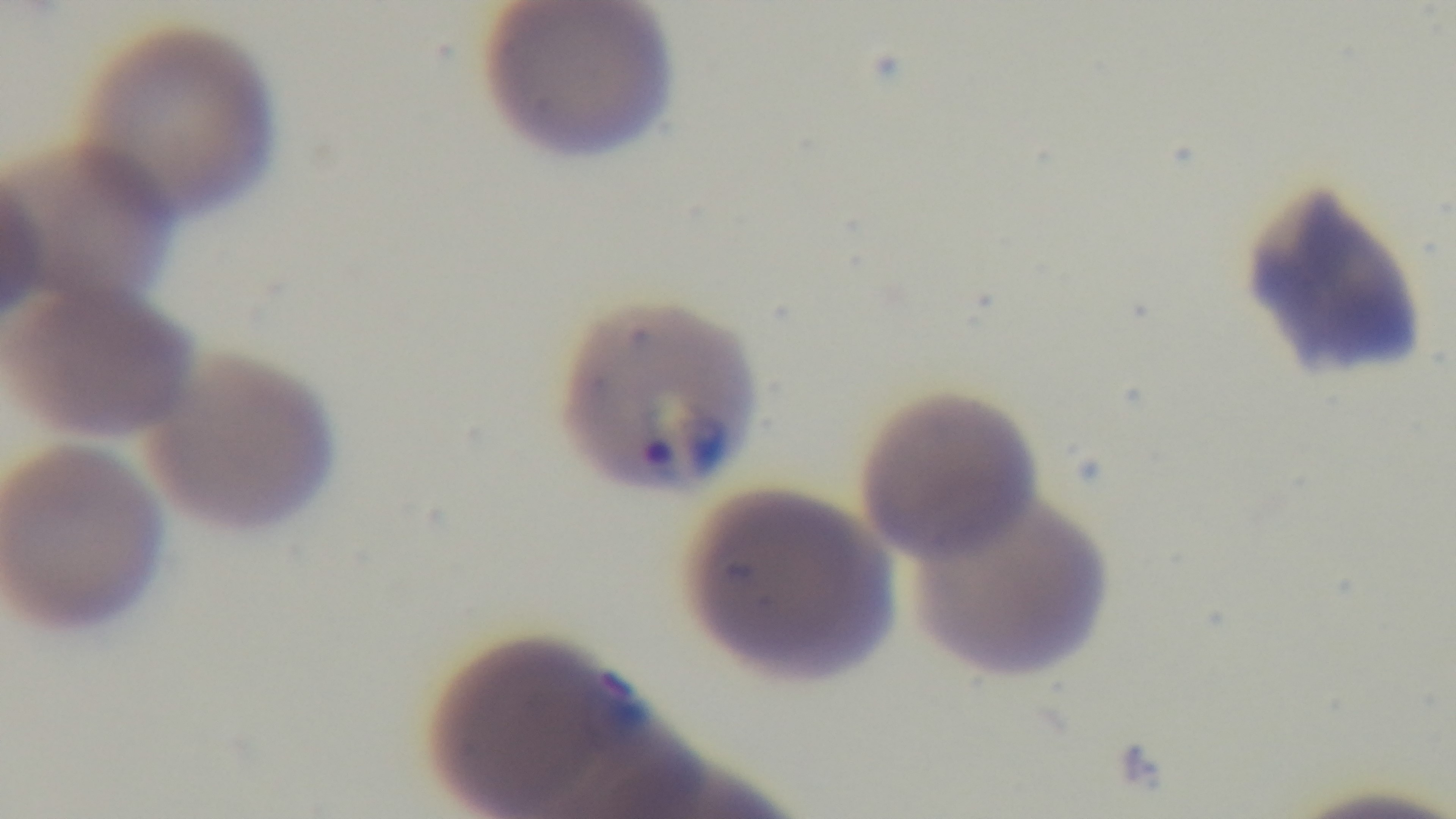
Summary:
  - Capture: mounted 4K digital camera
  - Malaria status: positive
  - Modality: light microscopy
  - Preparation: thin
  - Stain: Giemsa
  - Objective: 100x oil immersion
  - Field of view: one from the slide